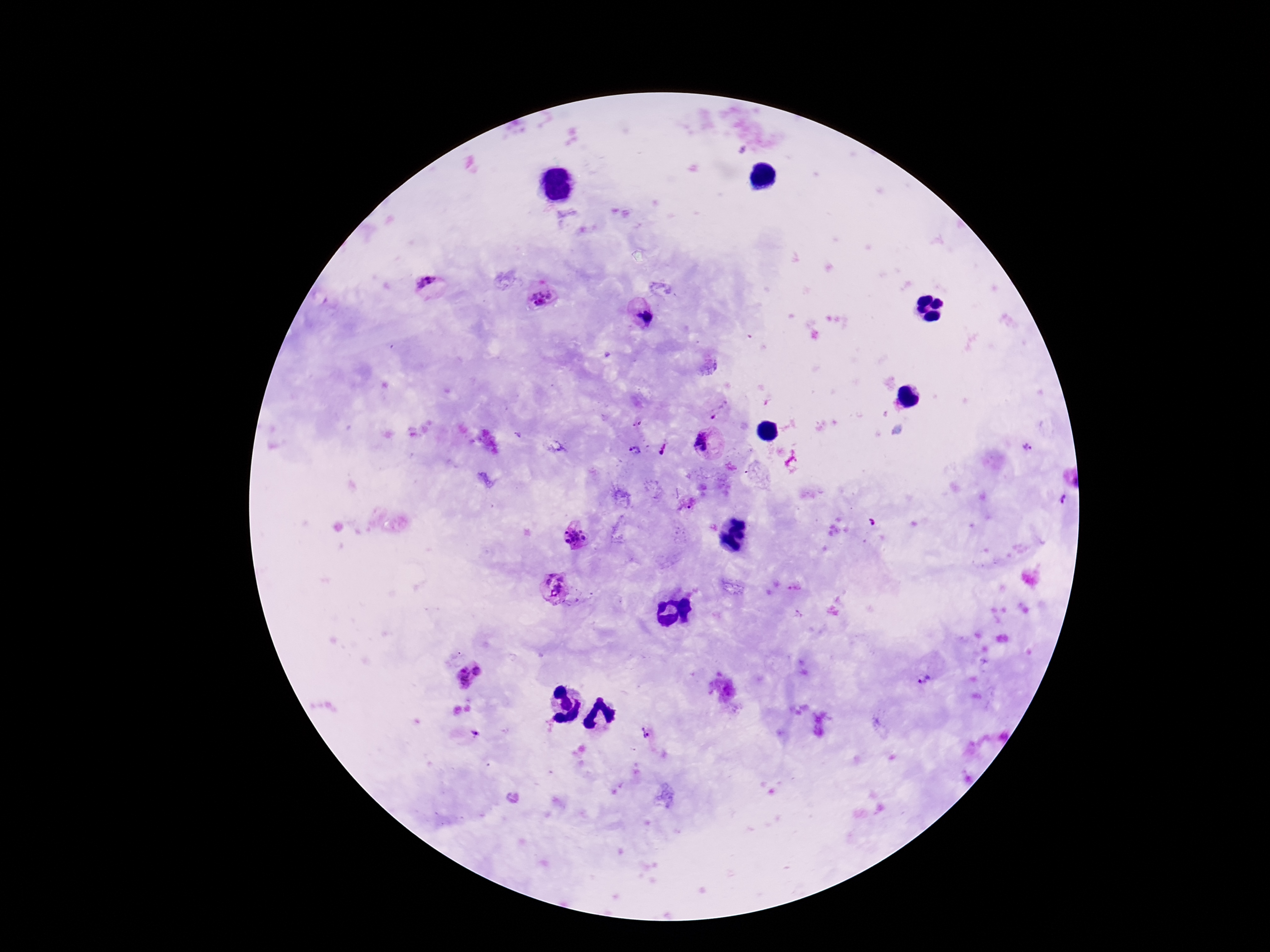

Approximate centers as [x, y] in pixels. Plasmodium parasite locations: [426, 286], [541, 298], [640, 314], [720, 411], [707, 444], [1028, 449], [664, 450], [634, 451], [1062, 501], [686, 506], [574, 537], [555, 587], [468, 675], [926, 677], [650, 732], [476, 734]. Image is 1270×952 pixels. Smartphone photograph taken through the microscope eyepiece. Patient malaria status: positive. Single field of view. 100x magnification. Giemsa stain. Thick peripheral-blood smear.